Outline each Plasmodium falciparum-infected red blood cell.
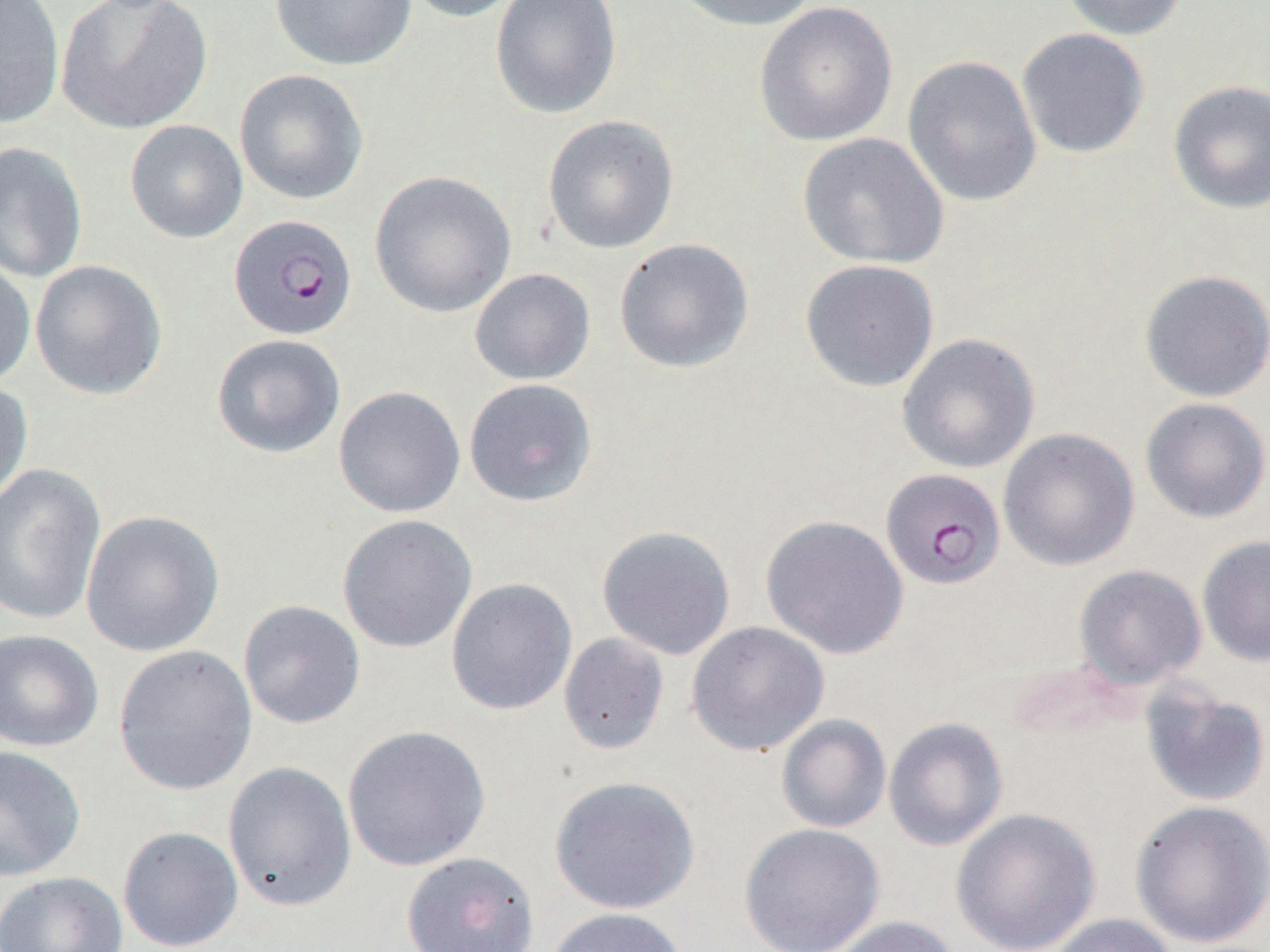

Approximate bounding boxes as (x1,y1)-(x2,y2) corner pairs in pixels.
Plasmodium falciparum-infected red blood cells: (229,214)-(358,340), (881,468)-(1005,589).

Uninfected red blood cell locations: (55,0)-(213,135), (270,0)-(418,72), (398,0)-(528,23), (490,0)-(622,120), (668,0)-(822,32), (1057,0)-(1190,41), (0,1)-(65,128), (754,2)-(897,146), (1016,27)-(1150,158), (902,55)-(1042,207), (234,69)-(369,205), (1167,80)-(1270,215), (542,115)-(679,254), (124,120)-(248,243), (797,133)-(949,269), (0,141)-(88,283), (368,170)-(516,318), (613,238)-(754,373), (0,256)-(36,390), (29,259)-(167,400), (799,259)-(940,393), (469,268)-(595,386), (1139,270)-(1270,403), (897,333)-(1040,474), (211,334)-(346,459), (464,378)-(598,507), (0,380)-(33,509), (333,386)-(466,518), (1139,397)-(1270,523), (998,428)-(1140,571), (0,465)-(106,625), (80,509)-(225,657), (337,514)-(477,653), (761,515)-(909,659), (596,525)-(736,660), (1197,535)-(1270,667), (1073,564)-(1206,689), (446,578)-(577,715), (238,600)-(366,729), (686,621)-(830,756), (0,629)-(104,752), (559,632)-(670,755), (113,645)-(257,796), (1139,680)-(1270,809), (776,714)-(891,833), (883,717)-(1008,851), (342,724)-(491,872), (0,745)-(87,882), (223,761)-(357,911), (549,775)-(700,915), (1129,799)-(1270,949), (951,808)-(1101,952), (739,823)-(885,952), (117,825)-(243,952), (400,851)-(541,952), (0,871)-(128,952), (543,907)-(689,952), (1045,913)-(1177,952), (827,916)-(962,952). Slide-level diagnosis: Plasmodium falciparum. Thin blood film. Image is 1270×952 pixels. Light microscopy. One field of a larger specimen. 1000x magnification.